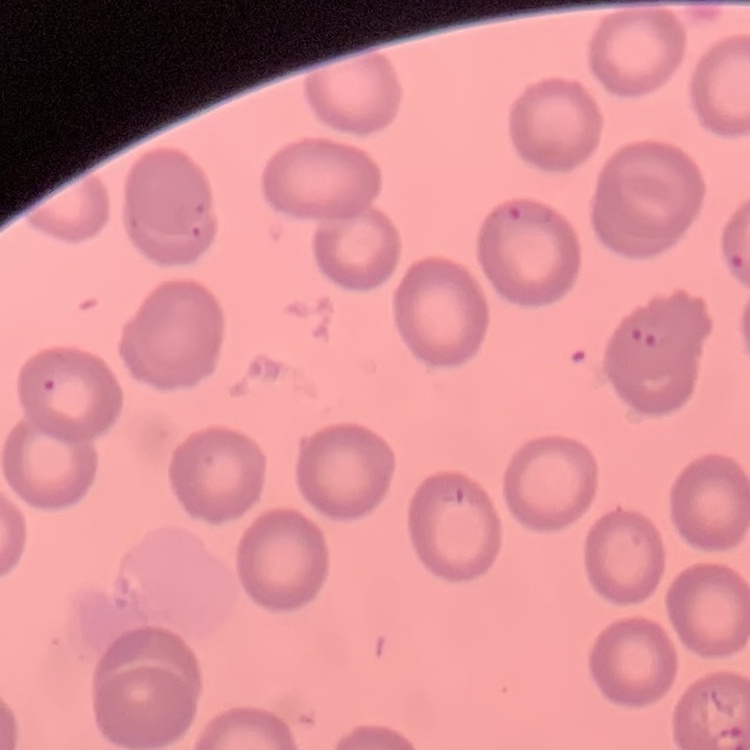
Summary:
  - Erythrocyte morphology: no rouleaux formation
  - Preparation: thin blood smear
  - Stain: Field's or Giemsa
  - Image type: one tile cut from a larger photomicrograph